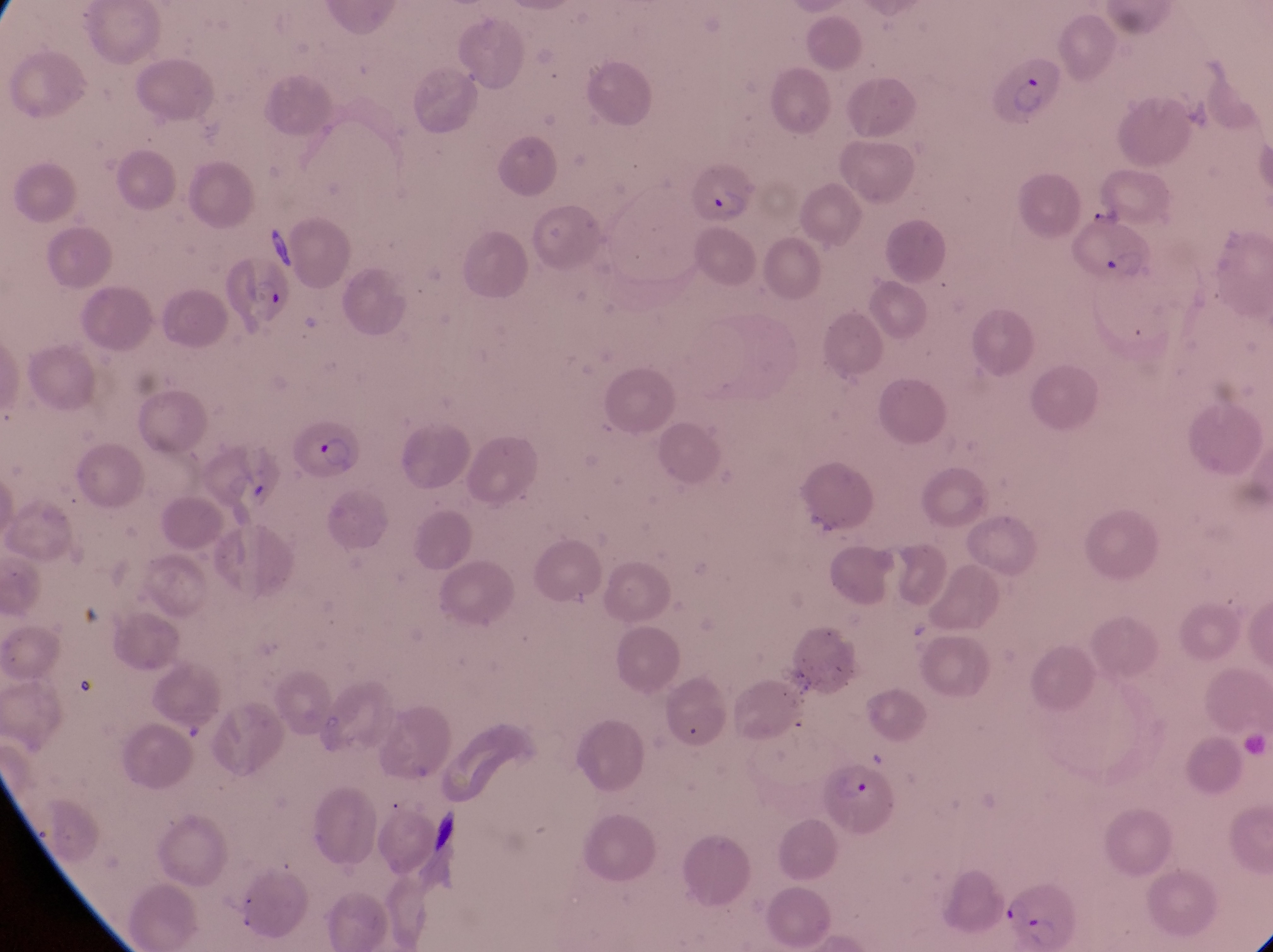
Approximate bounding boxes as {left, top, right, bottom} in pixels. Parasitised red blood cell locations: {995, 63, 1075, 137}, {689, 162, 754, 227}, {1069, 222, 1151, 289}, {215, 262, 295, 327}, {292, 415, 366, 482}, {822, 754, 891, 832}, {1003, 872, 1080, 949}. Photographed through the eyepiece of an Olympus CX-23 microscope with a smartphone camera. Collected in Uganda. Single field of view. Image is 1273×952 pixels. Magnification of 1000x. Thin blood film.